Outline each Plasmodium falciparum-infected red blood cell.
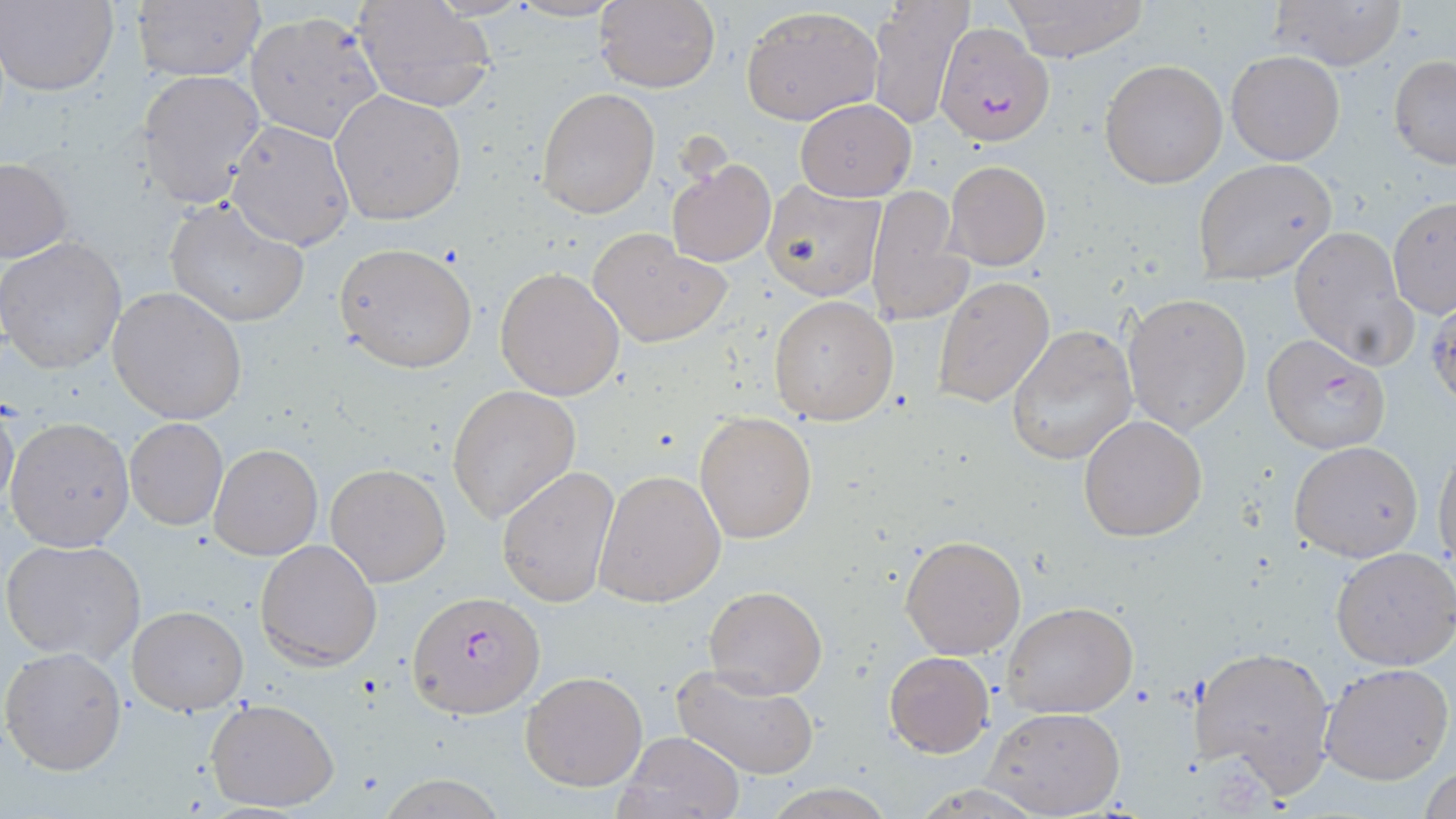
Approximate bounding boxes as (x1,y1)-(x2,y2) corner pairs in pixels.
Plasmodium falciparum-infected red blood cells: (936,21)-(1055,146), (1260,333)-(1392,453), (409,590)-(544,718).

Uninfected red blood cell locations: (594,0)-(721,92), (867,0)-(973,129), (1000,0)-(1150,62), (1268,0)-(1405,70), (2,1)-(118,96), (133,1)-(264,82), (353,1)-(495,112), (741,6)-(882,125), (245,11)-(385,145), (1225,49)-(1344,164), (1390,56)-(1456,168), (1099,59)-(1228,188), (139,72)-(266,206), (537,88)-(659,218), (330,90)-(466,227), (795,99)-(916,201), (226,119)-(357,251), (0,158)-(72,264), (666,158)-(775,267), (1192,159)-(1338,285), (945,160)-(1052,270), (762,180)-(885,301), (866,185)-(971,326), (1389,195)-(1456,317), (162,199)-(308,327), (1289,226)-(1415,368), (590,231)-(730,347), (1,236)-(127,372), (334,242)-(478,373), (494,266)-(624,401), (933,276)-(1054,408), (108,287)-(248,425), (1426,291)-(1456,410), (1123,292)-(1253,437), (768,294)-(899,426), (1007,325)-(1138,465), (448,385)-(580,524), (0,398)-(20,519), (695,411)-(817,543), (1077,415)-(1207,540), (5,418)-(134,553), (125,418)-(228,530), (1288,440)-(1422,562), (209,443)-(322,559), (1432,446)-(1455,572), (325,462)-(452,587), (497,463)-(621,609), (594,469)-(726,607), (900,532)-(1027,659), (2,537)-(147,664), (255,539)-(382,670), (1330,546)-(1456,669), (702,584)-(827,699), (1002,603)-(1137,718), (128,605)-(248,715), (1190,644)-(1339,797), (2,646)-(127,775), (883,651)-(994,757), (1320,661)-(1454,785), (672,664)-(822,780), (521,670)-(647,791), (206,697)-(340,813), (984,706)-(1125,817), (615,730)-(744,819), (1420,764)-(1455,819). Slide-level diagnosis: Plasmodium falciparum. Thin blood smear. Optical microscopy. Single field of view. Image is 1456×819 pixels. May-Grünwald-Giemsa stain. 1000x magnification.